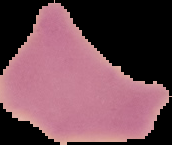

From a thin blood smear. Segmented cell region on a black background. Image is 172×145 pixels. Result: no Plasmodium parasites detected.